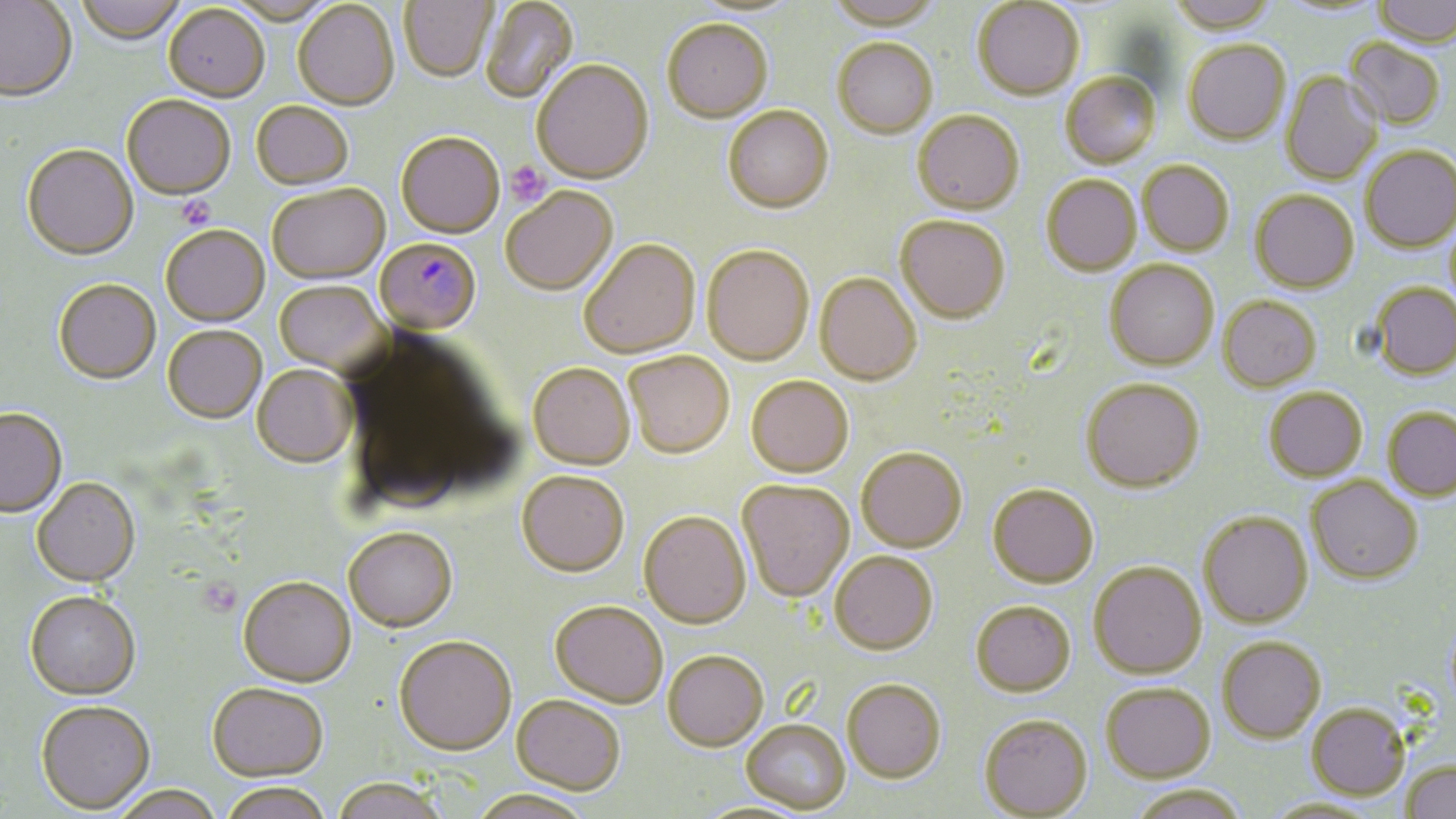

Approximate bounding boxes as [x1, y1, x2, y2] in pixels. Uninfected red blood cell locations: [0, 0, 78, 105], [74, 0, 188, 47], [399, 0, 498, 84], [481, 0, 579, 105], [826, 0, 945, 34], [1168, 0, 1278, 37], [1373, 0, 1456, 49], [224, 1, 339, 26], [685, 1, 805, 20], [972, 1, 1084, 103], [1275, 1, 1388, 21], [293, 2, 400, 113], [163, 7, 269, 105], [662, 23, 773, 126], [1343, 40, 1445, 130], [833, 41, 938, 141], [1184, 42, 1291, 146], [532, 62, 655, 187], [1281, 72, 1383, 186], [1060, 74, 1162, 171], [122, 97, 235, 202], [251, 103, 353, 191], [723, 108, 834, 217], [912, 113, 1024, 218], [397, 136, 504, 240], [1360, 146, 1456, 254], [21, 147, 138, 263], [1138, 162, 1233, 257], [1041, 176, 1141, 278], [268, 185, 391, 287], [501, 190, 618, 298], [1250, 191, 1359, 294], [895, 218, 1010, 327], [161, 228, 270, 329], [580, 241, 701, 361], [702, 248, 814, 368], [1105, 261, 1219, 372], [814, 275, 922, 388], [54, 281, 161, 386], [1372, 283, 1456, 380], [274, 284, 388, 378], [1218, 297, 1321, 393], [163, 328, 266, 426], [623, 354, 734, 461], [528, 365, 636, 473], [251, 367, 356, 470], [746, 377, 855, 480], [1081, 380, 1204, 494], [1265, 388, 1367, 482], [1383, 407, 1456, 501], [0, 410, 67, 519], [856, 450, 968, 554], [516, 474, 629, 581], [1306, 476, 1422, 584], [32, 480, 140, 589], [737, 483, 855, 604], [987, 486, 1099, 590], [1199, 511, 1313, 628], [638, 513, 752, 631], [343, 530, 458, 635], [829, 554, 938, 657], [1089, 563, 1207, 680], [238, 579, 356, 691], [25, 594, 141, 702], [970, 602, 1076, 698], [550, 603, 667, 711], [1217, 636, 1326, 742], [394, 639, 516, 759], [663, 653, 769, 755], [842, 681, 946, 785], [1101, 684, 1215, 783], [207, 686, 328, 785], [511, 697, 625, 799], [36, 703, 155, 816], [1306, 703, 1410, 800], [979, 716, 1093, 819], [742, 722, 851, 816], [1400, 759, 1456, 819], [332, 780, 447, 819], [1129, 783, 1249, 819], [218, 786, 333, 819], [110, 787, 224, 819], [468, 793, 594, 819], [1263, 798, 1383, 818], [690, 802, 816, 819]. Platelet locations: [505, 160, 549, 206], [175, 197, 215, 232]. Plasmodium falciparum-infected red blood cell locations: [375, 239, 481, 338]. Slide-level diagnosis: Plasmodium falciparum. Light microscopy. Image is 1456×819 pixels. One field of a larger specimen. May-Grünwald-Giemsa stain. Captured at 1000x magnification. Thin blood film.